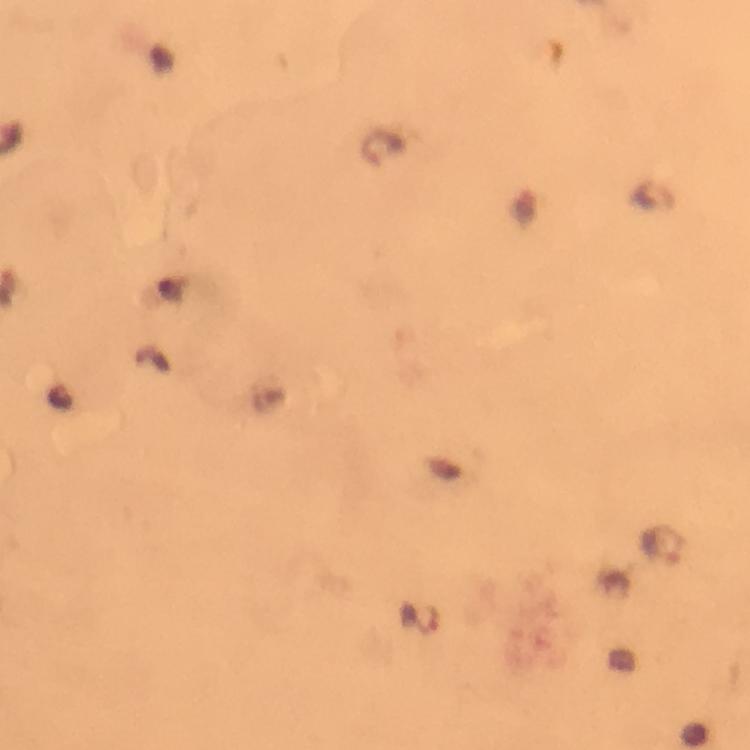

Approximate centers as (x, y) in pixels. Plasmodium parasite locations: (382, 148), (151, 359), (661, 545), (420, 620). A crop from one field of view. Giemsa stain. Smartphone photograph taken through a microscope. Thick blood film. Image is 750×750 pixels. Immersion oil was used. From a malaria diagnostic workup. 100x magnification.